Identify the cell.
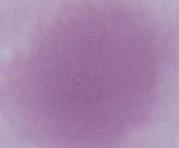

This is an erythrocyte.

Summary:
  - Modality: micrograph
  - Magnification: 1000x